Locate and identify every blood parasite.
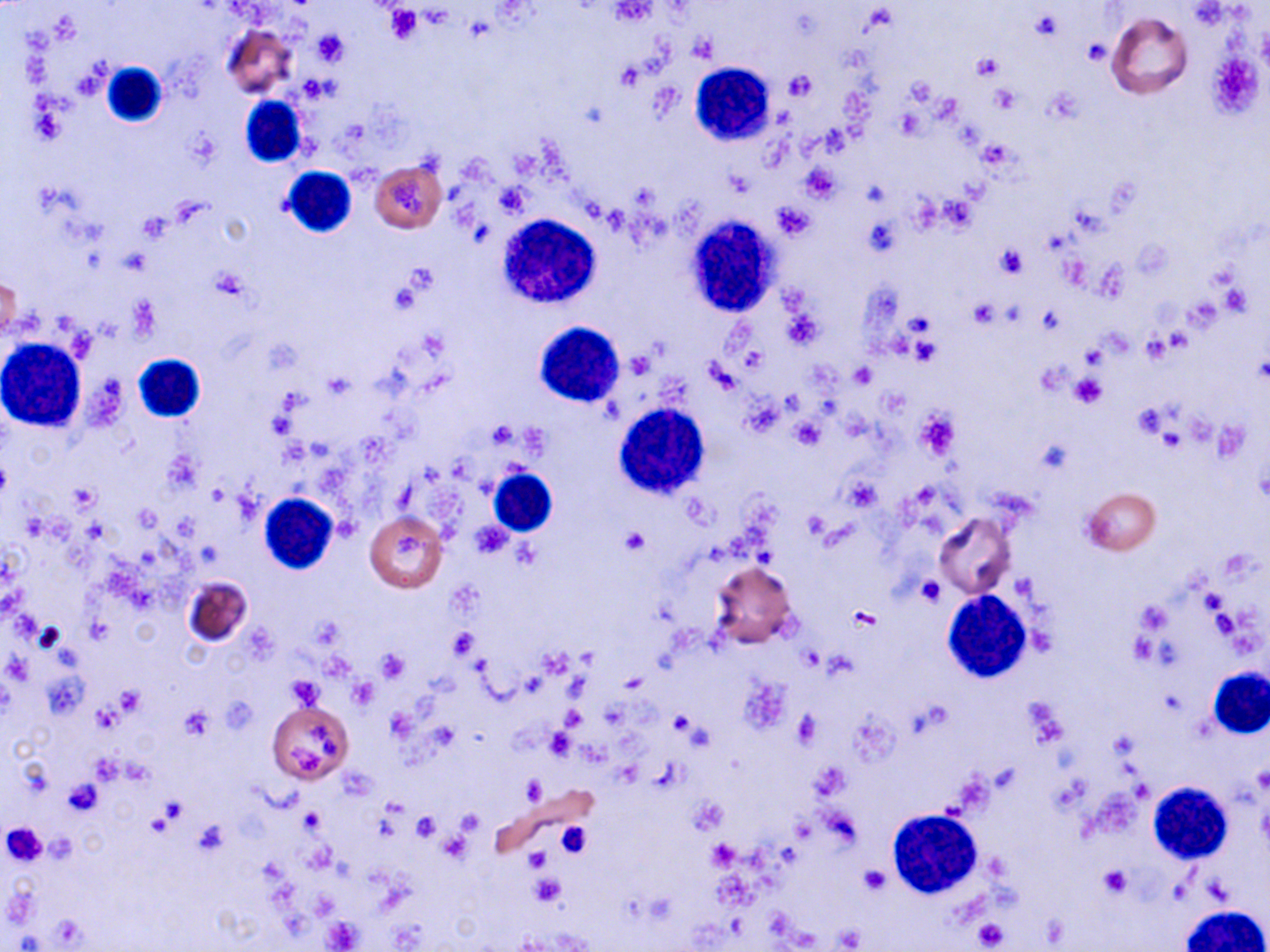
No blood parasites seen.

Approximate bounding boxes as (x1, y1, x2, y2) in pixels. Platelet locations: (607, 2, 656, 26), (384, 6, 422, 43), (1032, 11, 1064, 40), (312, 29, 348, 66), (689, 33, 717, 62), (1085, 39, 1112, 63), (971, 52, 1003, 81), (616, 65, 644, 90), (784, 71, 816, 101), (907, 77, 939, 105), (989, 84, 1021, 112), (896, 107, 924, 138), (185, 130, 220, 168), (802, 166, 840, 201), (394, 180, 423, 214), (495, 184, 530, 215), (939, 197, 976, 231), (773, 203, 815, 239), (139, 212, 173, 241), (995, 246, 1029, 278), (210, 270, 248, 302), (387, 280, 420, 314), (1221, 282, 1251, 314), (970, 300, 999, 328), (782, 307, 822, 349), (910, 337, 941, 366), (628, 351, 653, 378), (851, 364, 875, 387), (1070, 374, 1107, 409), (1130, 395, 1175, 440), (915, 410, 960, 461), (790, 417, 826, 448), (843, 476, 881, 512), (69, 483, 99, 511), (620, 527, 652, 556), (392, 533, 432, 566), (917, 575, 947, 605), (1200, 590, 1226, 617), (1136, 602, 1172, 636), (849, 608, 880, 630), (450, 630, 478, 659), (377, 650, 409, 683), (287, 676, 324, 709), (349, 679, 377, 708), (117, 687, 144, 716), (93, 703, 123, 731), (180, 708, 213, 739), (386, 709, 417, 740), (670, 711, 699, 736), (792, 711, 821, 746), (309, 725, 338, 757), (544, 727, 574, 760), (292, 749, 322, 772), (1253, 765, 1269, 794), (522, 777, 546, 802), (63, 779, 104, 816), (690, 797, 727, 833), (411, 813, 439, 840), (555, 820, 592, 858), (192, 821, 229, 856), (0, 822, 48, 867), (709, 840, 738, 868), (525, 850, 551, 872), (860, 866, 889, 894), (1099, 867, 1131, 896), (531, 875, 565, 906), (325, 919, 359, 949), (974, 919, 1006, 950), (836, 926, 864, 950). White blood cell locations: (102, 61, 168, 128), (692, 66, 775, 148), (241, 96, 306, 167), (281, 167, 356, 238), (500, 214, 601, 307), (686, 219, 782, 317), (537, 324, 623, 403), (0, 338, 87, 431), (133, 354, 208, 423), (616, 403, 709, 497), (488, 467, 558, 537), (258, 493, 338, 574), (942, 591, 1032, 683), (1209, 667, 1269, 739), (1147, 783, 1228, 865), (887, 808, 981, 899), (1180, 905, 1267, 952). Uninfected red blood cell locations: (1106, 12, 1193, 99), (223, 26, 297, 100), (370, 161, 446, 232), (1, 275, 22, 340), (1083, 486, 1161, 555), (365, 512, 447, 593), (934, 512, 1016, 598), (709, 561, 799, 651), (183, 576, 254, 649), (268, 703, 353, 781). Slide-level diagnosis: negative for blood parasites. Optical microscopy. Single field of view. May-Grünwald-Giemsa stain. Image is 1270×952 pixels. Captured at 1000x magnification. Thin blood smear.